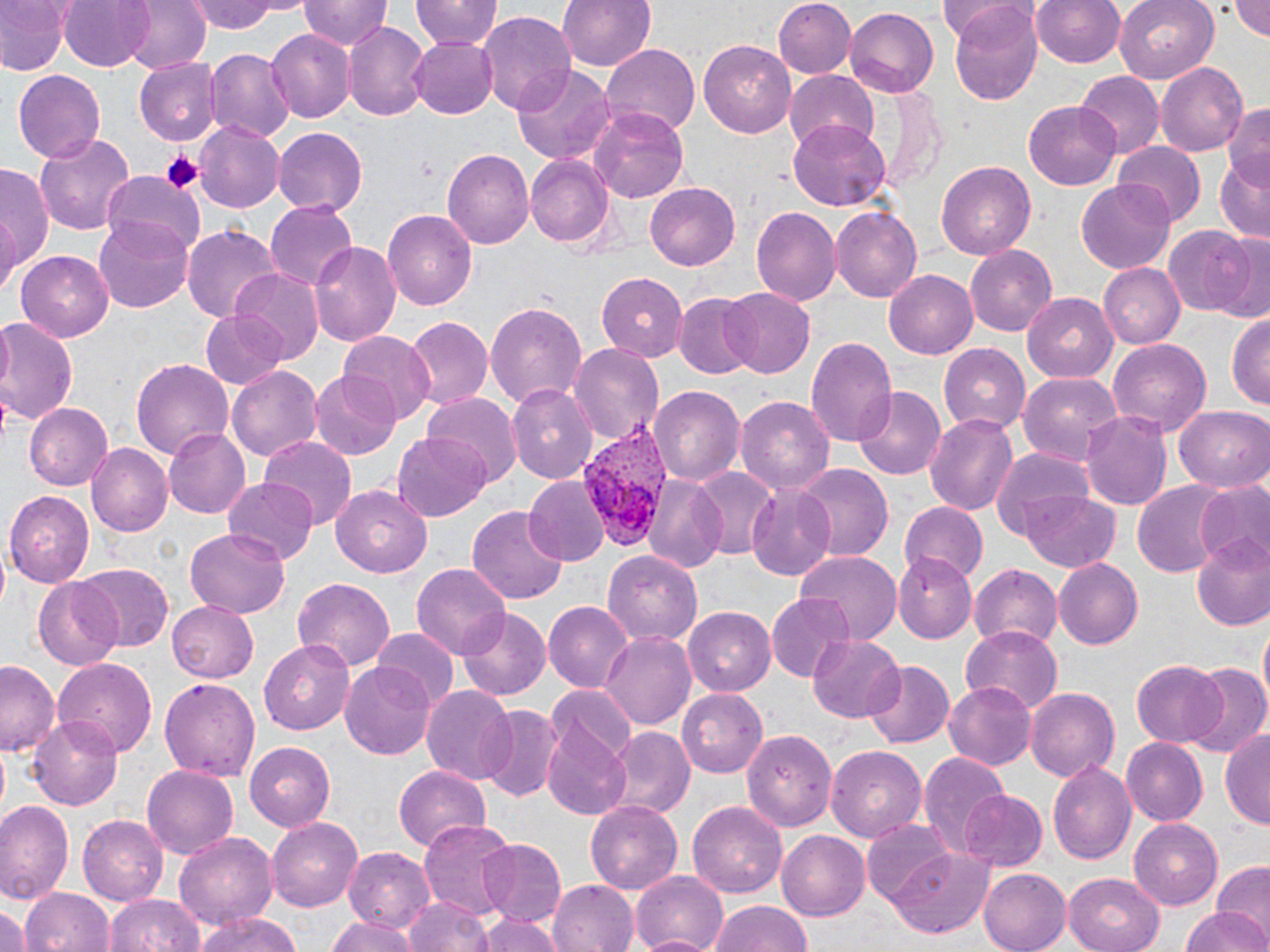

plasmodium_vivax_infected_red_blood_cell_locations: 'approximate bounding boxes as named x1/y1/x2/y2 corners in pixels: (x1=568, y1=429, x2=668, y2=554)'
slide_level_diagnosis: Plasmodium vivax
stain: May-Grünwald-Giemsa
magnification: 1000x
platelet_locations: 'approximate bounding boxes as named x1/y1/x2/y2 corners in pixels: (x1=161, y1=150, x2=201, y2=195)'
field_of_view: single
modality: light microscopy
preparation: thin blood film
image_size: 1270×952 pixels
uninfected_red_blood_cell_locations: 'approximate bounding boxes as named x1/y1/x2/y2 corners in pixels: (x1=0, y1=0, x2=68, y2=75), (x1=58, y1=0, x2=154, y2=71), (x1=120, y1=0, x2=211, y2=73), (x1=188, y1=0, x2=296, y2=34), (x1=412, y1=0, x2=501, y2=53), (x1=557, y1=0, x2=657, y2=74), (x1=774, y1=0, x2=857, y2=77), (x1=1030, y1=0, x2=1128, y2=68), (x1=1114, y1=0, x2=1219, y2=83), (x1=1229, y1=0, x2=1270, y2=41), (x1=300, y1=1, x2=390, y2=53), (x1=941, y1=1, x2=1034, y2=40), (x1=948, y1=3, x2=1044, y2=106), (x1=842, y1=8, x2=940, y2=100), (x1=476, y1=11, x2=578, y2=115), (x1=565, y1=14, x2=682, y2=119), (x1=345, y1=22, x2=431, y2=122), (x1=266, y1=28, x2=355, y2=124), (x1=411, y1=35, x2=498, y2=118), (x1=701, y1=39, x2=800, y2=138), (x1=601, y1=44, x2=699, y2=136), (x1=204, y1=48, x2=293, y2=142), (x1=137, y1=58, x2=222, y2=145), (x1=1155, y1=62, x2=1248, y2=158), (x1=512, y1=65, x2=617, y2=162), (x1=10, y1=69, x2=106, y2=164), (x1=784, y1=72, x2=880, y2=155), (x1=1074, y1=73, x2=1161, y2=158), (x1=870, y1=83, x2=945, y2=189), (x1=1223, y1=100, x2=1270, y2=181), (x1=1024, y1=102, x2=1120, y2=190), (x1=591, y1=105, x2=689, y2=204), (x1=790, y1=119, x2=892, y2=209), (x1=193, y1=122, x2=284, y2=213), (x1=272, y1=127, x2=367, y2=215), (x1=34, y1=131, x2=136, y2=239), (x1=1113, y1=142, x2=1206, y2=227), (x1=443, y1=148, x2=533, y2=250), (x1=525, y1=154, x2=614, y2=249), (x1=1214, y1=155, x2=1270, y2=241), (x1=935, y1=160, x2=1036, y2=260), (x1=0, y1=163, x2=55, y2=276), (x1=100, y1=172, x2=205, y2=263), (x1=1076, y1=182, x2=1177, y2=273), (x1=645, y1=183, x2=740, y2=269), (x1=263, y1=201, x2=358, y2=293), (x1=830, y1=205, x2=922, y2=302), (x1=750, y1=206, x2=841, y2=309), (x1=383, y1=209, x2=478, y2=309), (x1=95, y1=216, x2=196, y2=312), (x1=181, y1=223, x2=282, y2=324), (x1=1161, y1=226, x2=1256, y2=317), (x1=1214, y1=232, x2=1269, y2=323), (x1=312, y1=240, x2=402, y2=349), (x1=965, y1=245, x2=1057, y2=335), (x1=16, y1=250, x2=118, y2=341), (x1=1099, y1=263, x2=1184, y2=347), (x1=230, y1=268, x2=326, y2=364), (x1=884, y1=269, x2=977, y2=358), (x1=597, y1=271, x2=689, y2=362), (x1=720, y1=286, x2=816, y2=378), (x1=1023, y1=294, x2=1119, y2=382), (x1=674, y1=295, x2=758, y2=377), (x1=484, y1=300, x2=589, y2=413), (x1=200, y1=309, x2=289, y2=389), (x1=1228, y1=313, x2=1270, y2=412), (x1=403, y1=316, x2=492, y2=411), (x1=0, y1=321, x2=79, y2=428), (x1=341, y1=330, x2=435, y2=419), (x1=805, y1=336, x2=897, y2=450), (x1=1109, y1=338, x2=1211, y2=434), (x1=570, y1=343, x2=664, y2=448), (x1=941, y1=343, x2=1033, y2=436), (x1=130, y1=358, x2=235, y2=460), (x1=227, y1=364, x2=324, y2=464), (x1=309, y1=369, x2=402, y2=462), (x1=1017, y1=372, x2=1123, y2=465), (x1=646, y1=384, x2=744, y2=486), (x1=506, y1=386, x2=596, y2=484), (x1=852, y1=388, x2=944, y2=480), (x1=422, y1=395, x2=520, y2=488), (x1=736, y1=395, x2=835, y2=495), (x1=25, y1=402, x2=114, y2=489), (x1=1176, y1=407, x2=1269, y2=491), (x1=1080, y1=411, x2=1171, y2=508), (x1=923, y1=412, x2=1018, y2=516), (x1=165, y1=427, x2=252, y2=518), (x1=391, y1=430, x2=491, y2=521), (x1=259, y1=436, x2=358, y2=533), (x1=88, y1=442, x2=172, y2=534), (x1=990, y1=447, x2=1093, y2=540), (x1=795, y1=463, x2=892, y2=560), (x1=692, y1=468, x2=780, y2=562), (x1=643, y1=475, x2=727, y2=571), (x1=524, y1=477, x2=608, y2=567), (x1=222, y1=478, x2=318, y2=563), (x1=1134, y1=480, x2=1226, y2=578), (x1=1195, y1=483, x2=1270, y2=572), (x1=745, y1=484, x2=840, y2=580), (x1=330, y1=485, x2=433, y2=576), (x1=5, y1=490, x2=96, y2=586), (x1=1022, y1=493, x2=1119, y2=570), (x1=897, y1=502, x2=987, y2=584), (x1=468, y1=503, x2=568, y2=607), (x1=185, y1=529, x2=290, y2=619), (x1=1190, y1=535, x2=1270, y2=633), (x1=603, y1=549, x2=705, y2=646), (x1=795, y1=552, x2=901, y2=646), (x1=892, y1=552, x2=975, y2=643), (x1=1055, y1=559, x2=1144, y2=648), (x1=73, y1=562, x2=173, y2=653), (x1=412, y1=563, x2=513, y2=660), (x1=967, y1=563, x2=1064, y2=649), (x1=291, y1=577, x2=395, y2=674), (x1=33, y1=578, x2=127, y2=671), (x1=767, y1=595, x2=860, y2=680), (x1=168, y1=601, x2=258, y2=682), (x1=544, y1=601, x2=633, y2=692), (x1=682, y1=606, x2=776, y2=696), (x1=456, y1=607, x2=552, y2=700), (x1=959, y1=626, x2=1064, y2=716), (x1=369, y1=627, x2=459, y2=706), (x1=601, y1=631, x2=696, y2=731), (x1=808, y1=635, x2=903, y2=724), (x1=259, y1=640, x2=355, y2=735), (x1=53, y1=657, x2=158, y2=756), (x1=865, y1=659, x2=954, y2=749), (x1=1131, y1=659, x2=1229, y2=748), (x1=341, y1=661, x2=436, y2=760), (x1=0, y1=663, x2=60, y2=755), (x1=1186, y1=663, x2=1270, y2=758), (x1=160, y1=677, x2=262, y2=781), (x1=945, y1=680, x2=1036, y2=771), (x1=421, y1=686, x2=517, y2=784), (x1=548, y1=686, x2=640, y2=768), (x1=1025, y1=686, x2=1119, y2=782), (x1=677, y1=688, x2=769, y2=775), (x1=477, y1=707, x2=562, y2=802), (x1=29, y1=716, x2=123, y2=810), (x1=543, y1=720, x2=633, y2=820), (x1=1219, y1=726, x2=1270, y2=827), (x1=607, y1=728, x2=694, y2=817), (x1=744, y1=728, x2=838, y2=834), (x1=1121, y1=739, x2=1208, y2=826), (x1=245, y1=742, x2=335, y2=830), (x1=825, y1=745, x2=928, y2=841), (x1=920, y1=753, x2=1010, y2=858), (x1=1047, y1=761, x2=1136, y2=864), (x1=142, y1=766, x2=237, y2=859), (x1=392, y1=766, x2=490, y2=851), (x1=959, y1=789, x2=1048, y2=874), (x1=585, y1=799, x2=686, y2=893), (x1=688, y1=800, x2=787, y2=897), (x1=0, y1=801, x2=75, y2=904), (x1=77, y1=814, x2=169, y2=905), (x1=267, y1=818, x2=366, y2=911), (x1=419, y1=818, x2=518, y2=924), (x1=1129, y1=818, x2=1227, y2=910), (x1=863, y1=822, x2=959, y2=907), (x1=776, y1=831, x2=870, y2=919), (x1=173, y1=833, x2=278, y2=931), (x1=476, y1=837, x2=568, y2=927), (x1=344, y1=845, x2=437, y2=930), (x1=888, y1=845, x2=996, y2=938), (x1=1212, y1=861, x2=1270, y2=941), (x1=977, y1=868, x2=1070, y2=952), (x1=631, y1=870, x2=730, y2=952), (x1=1062, y1=874, x2=1164, y2=952), (x1=550, y1=877, x2=637, y2=952), (x1=22, y1=886, x2=114, y2=952), (x1=105, y1=894, x2=204, y2=952), (x1=404, y1=896, x2=495, y2=952), (x1=0, y1=899, x2=30, y2=952), (x1=704, y1=899, x2=815, y2=952), (x1=1179, y1=908, x2=1267, y2=952), (x1=196, y1=912, x2=306, y2=952), (x1=474, y1=913, x2=562, y2=952), (x1=325, y1=918, x2=423, y2=952)'